Assess this cell for malaria.
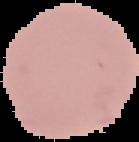
It is uninfected.

Summary:
  - Image size: 139×142 pixels
  - Image type: segmented cell region with the area outside set to black
  - Preparation: thin blood film